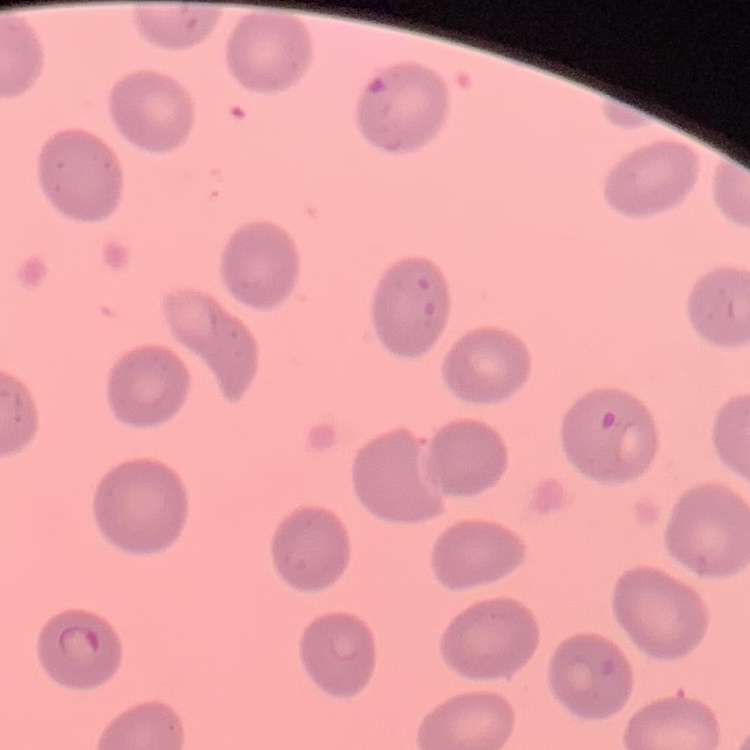
{
  "red_blood_cell_morphology": "no rouleaux formation",
  "image_type": "one tile cut from a larger photomicrograph",
  "stain": "Field's or Giemsa",
  "preparation": "thin blood film"
}